Report the malaria status of this cell.
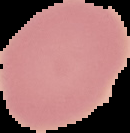

Uninfected.

From a thin blood smear. Image is 130×133 pixels. Segmented cell region on a black background.